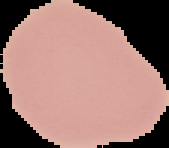

image type = cell region segmented out of the field of view; surrounding area masked to black
result = no Plasmodium parasites seen
image size = 169×148 pixels
preparation = thin blood smear